Report the malaria status of this cell.
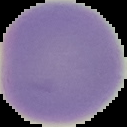
It is uninfected.

Cell region segmented out of the field of view; the surrounding area is masked to black. From a thin blood smear. Image is 127×127 pixels.